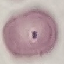
Summary:
  - Malaria status: uninfected
  - Image type: cell patch, automatically extracted from a larger field of view and resized to 64 × 64 pixels
  - Stain: Giemsa
  - Capture: smartphone through the microscope eyepiece
  - Preparation: thin smear